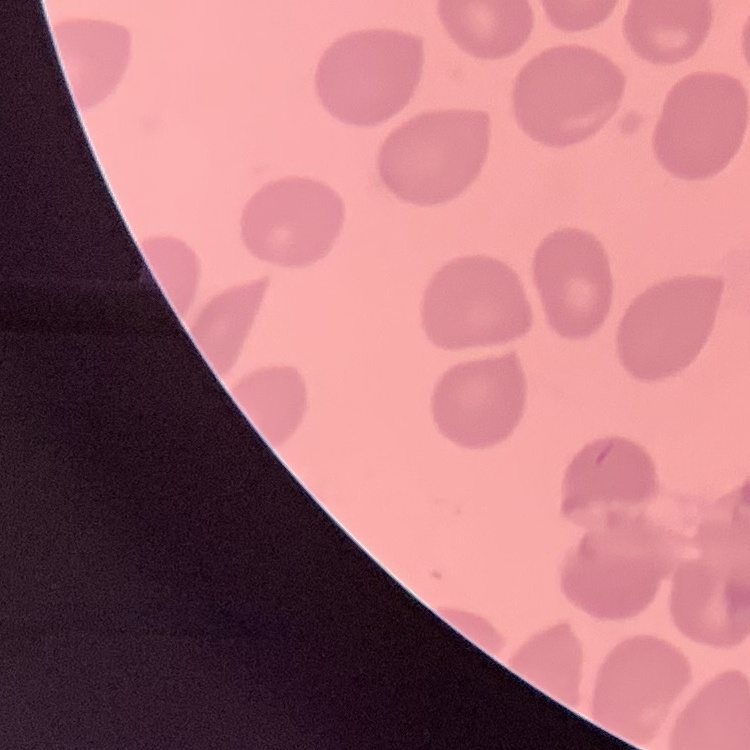

Summary:
  - Red blood cell morphology: no rouleaux formation
  - Stain: Field's or Giemsa
  - Preparation: thin peripheral smear
  - Image type: square crop of a larger photomicrograph